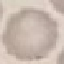

Summary:
  - Malaria status: uninfected
  - Preparation: thin blood film
  - Stain: Giemsa
  - Capture: smartphone camera at the microscope eyepiece
  - Image type: cell patch, automatically extracted from a larger field of view and resized to 64 × 64 pixels